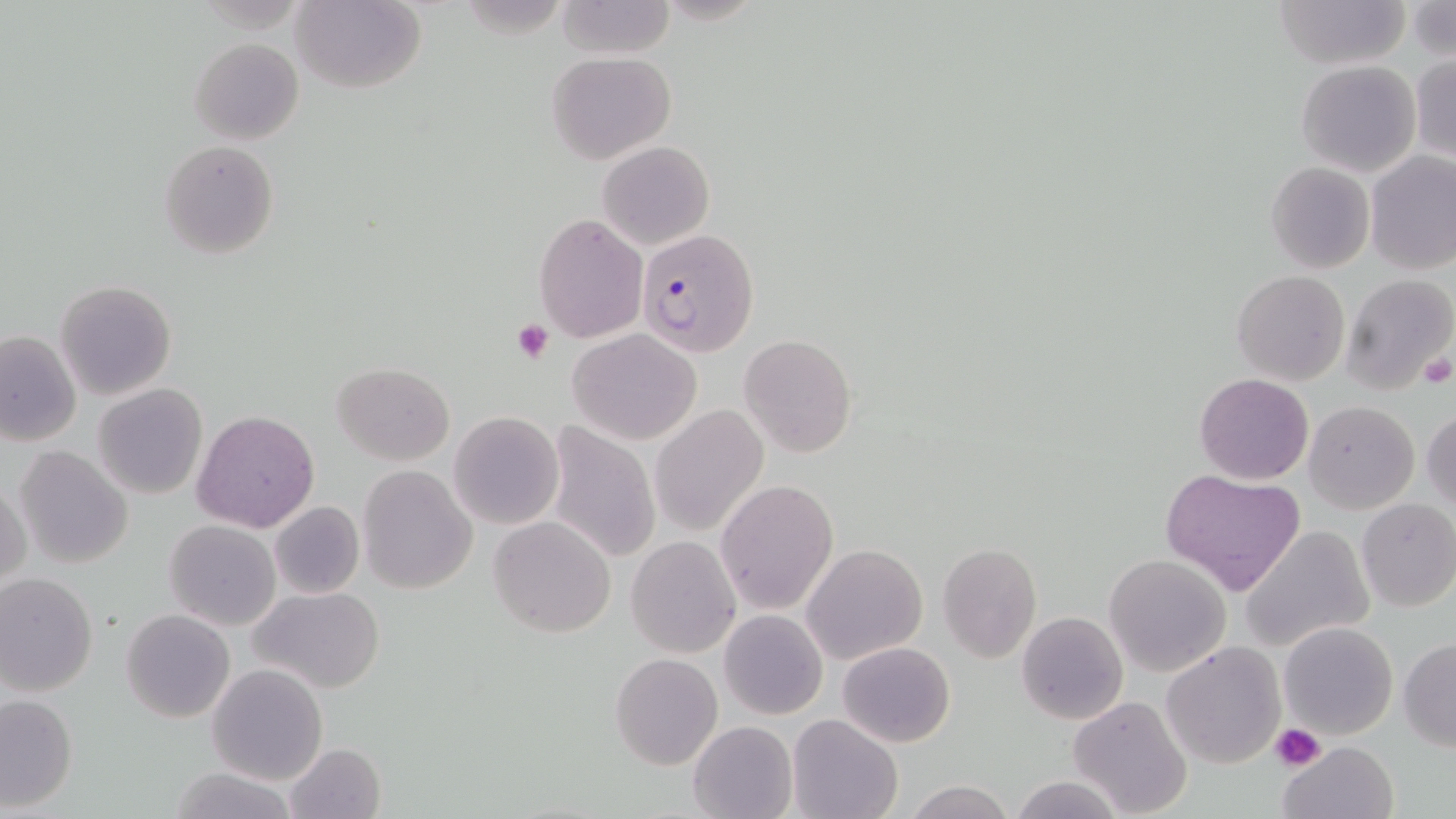
{
  "slide_level_diagnosis": "Plasmodium falciparum",
  "platelet_locations": "approximate bounding boxes as (x1,y1)-(x2,y2) corner pairs in pixels: (512,319)-(553,363), (1414,351)-(1453,391), (1270,723)-(1325,773)",
  "magnification": "1000x",
  "stain": "May-Grünwald-Giemsa",
  "field_of_view": "single",
  "modality": "optical microscopy",
  "uninfected_red_blood_cell_locations": "approximate bounding boxes as (x1,y1)-(x2,y2) corner pairs in pixels: (1270,0)-(1410,70), (291,1)-(425,92), (553,1)-(674,60), (1405,3)-(1455,60), (189,37)-(304,143), (544,52)-(676,163), (1409,53)-(1456,163), (1295,60)-(1421,177), (160,139)-(280,259), (598,140)-(714,251), (1365,151)-(1456,274), (1266,161)-(1375,274), (533,214)-(648,341), (1231,271)-(1350,386), (1341,272)-(1456,395), (55,279)-(178,400), (568,329)-(702,445), (1,330)-(80,447), (738,334)-(856,458), (333,363)-(455,463), (1195,373)-(1314,485), (92,383)-(209,499), (1304,399)-(1419,514), (651,404)-(768,538), (1421,404)-(1455,515), (192,409)-(319,533), (449,411)-(564,530), (545,422)-(662,565), (15,445)-(133,569), (357,464)-(477,594), (1159,467)-(1305,596), (1,477)-(29,592), (714,479)-(839,615), (1355,498)-(1456,612), (269,501)-(364,600), (488,516)-(616,638), (164,520)-(281,631), (1238,524)-(1375,652), (626,537)-(740,658), (801,543)-(928,663), (938,543)-(1041,662), (1104,554)-(1232,678), (0,572)-(97,694), (247,585)-(385,693), (121,609)-(236,723), (718,610)-(828,720), (1017,611)-(1129,724), (1279,620)-(1398,738), (1398,638)-(1456,751), (838,641)-(955,748), (1162,642)-(1286,769), (610,652)-(722,770), (205,662)-(329,784), (1069,671)-(1277,797), (1,693)-(78,812), (1068,696)-(1194,819), (786,713)-(903,819), (687,720)-(796,819), (1277,740)-(1398,819), (285,741)-(386,819), (166,765)-(302,819), (1009,774)-(1128,818), (902,779)-(1017,819)",
  "image_size": "1456×819 pixels",
  "plasmodium_falciparum_infected_red_blood_cell_locations": "approximate bounding boxes as (x1,y1)-(x2,y2) corner pairs in pixels: (636,227)-(759,356)",
  "preparation": "thin blood film"
}